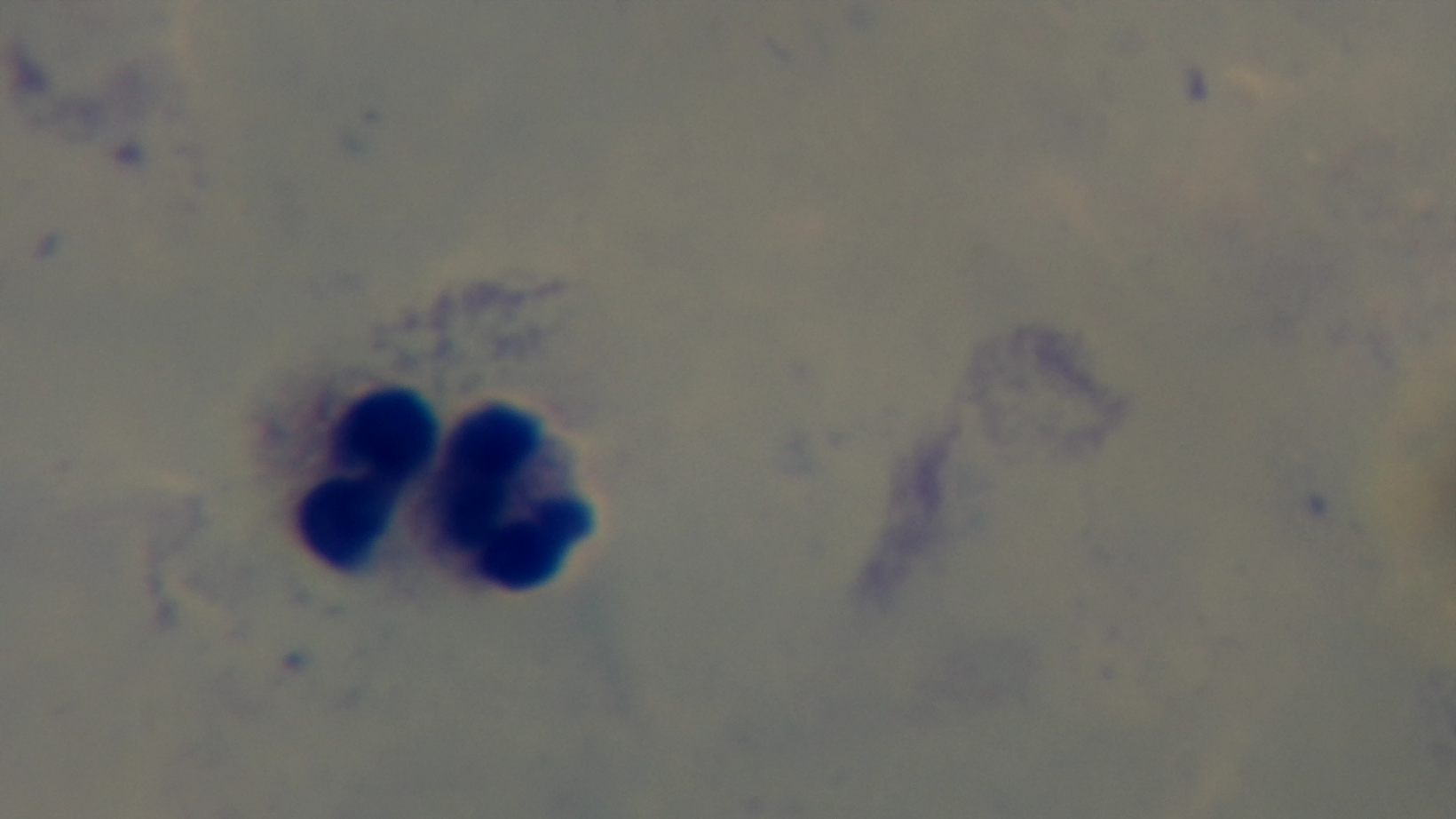

Summary:
  - Preparation: thick blood film
  - Stain: Giemsa
  - Field of view: one from the slide
  - Modality: light microscopy
  - Malaria status: negative
  - Objective: 100x oil immersion
  - Capture: mounted 4K digital camera